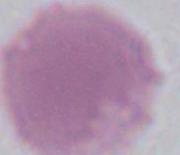
1000x magnification. Micrograph. An erythrocyte is seen.